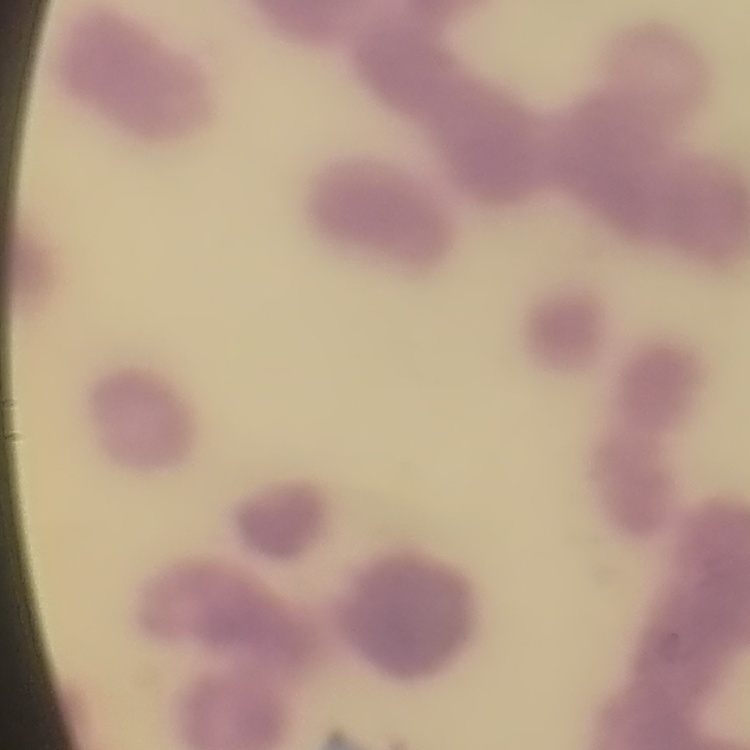
red blood cell morphology = rouleaux formation
image type = square crop of a larger photomicrograph
stain = Field's or Giemsa
preparation = thin blood film